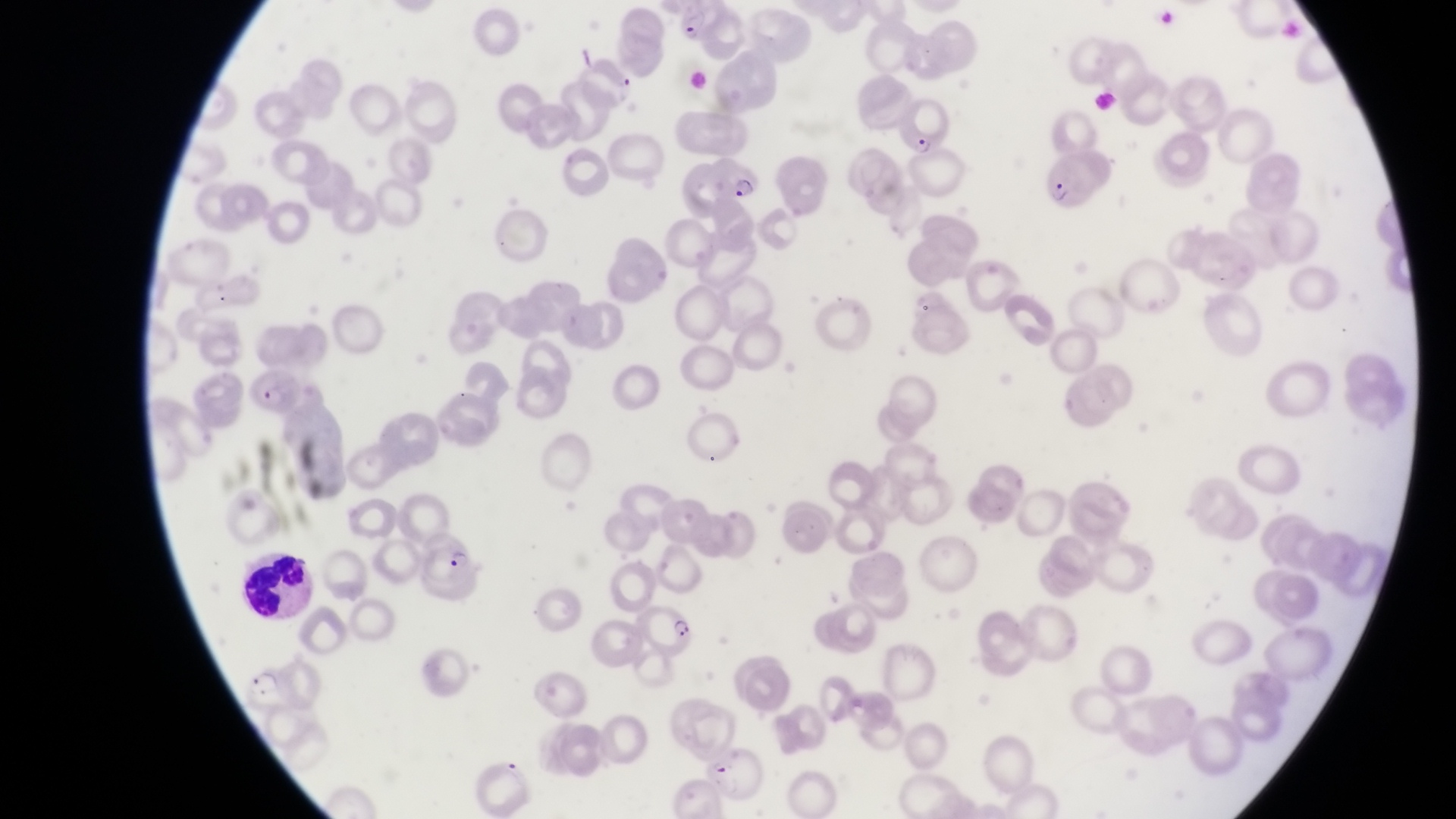
Approximate bounding boxes as [left, top, right, bottom] in pixels.
Summary:
  - Parasitised red blood cell locations: [898, 121, 945, 161], [1031, 142, 1113, 215], [711, 158, 764, 204], [248, 375, 308, 421], [406, 525, 473, 588], [631, 604, 702, 657], [230, 664, 291, 717]
  - Leukocyte locations: [232, 552, 324, 624]
  - Trophozoite locations: [676, 7, 713, 47]
  - Capture: smartphone photograph through the eyepiece of an Olympus CX-23 microscope
  - Magnification: 1000x
  - Country: Uganda
  - Preparation: thin blood film
  - Image size: 1456×819 pixels
  - Field of view: single